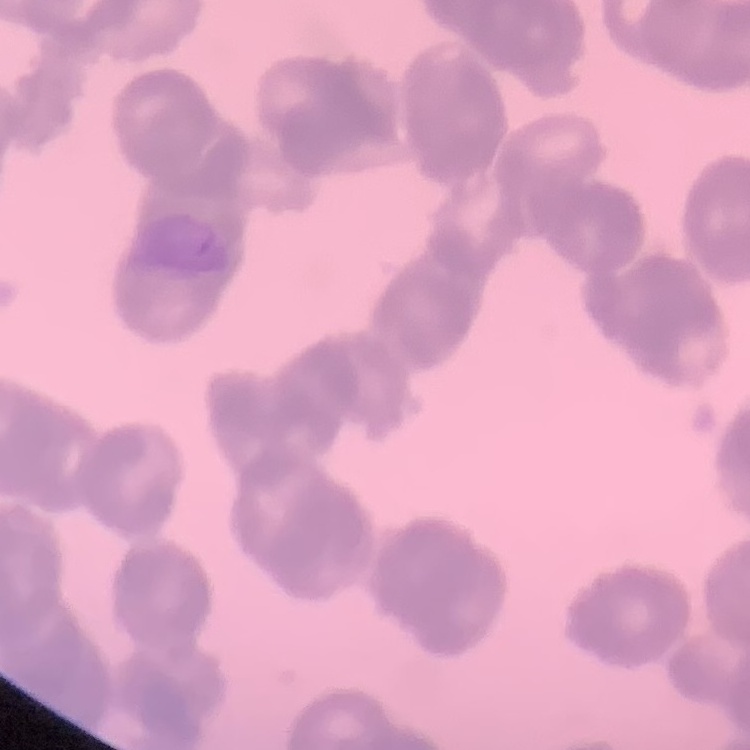

erythrocyte morphology = rouleaux formation
image type = square crop of a larger photomicrograph
stain = Field's or Giemsa
preparation = thin blood film